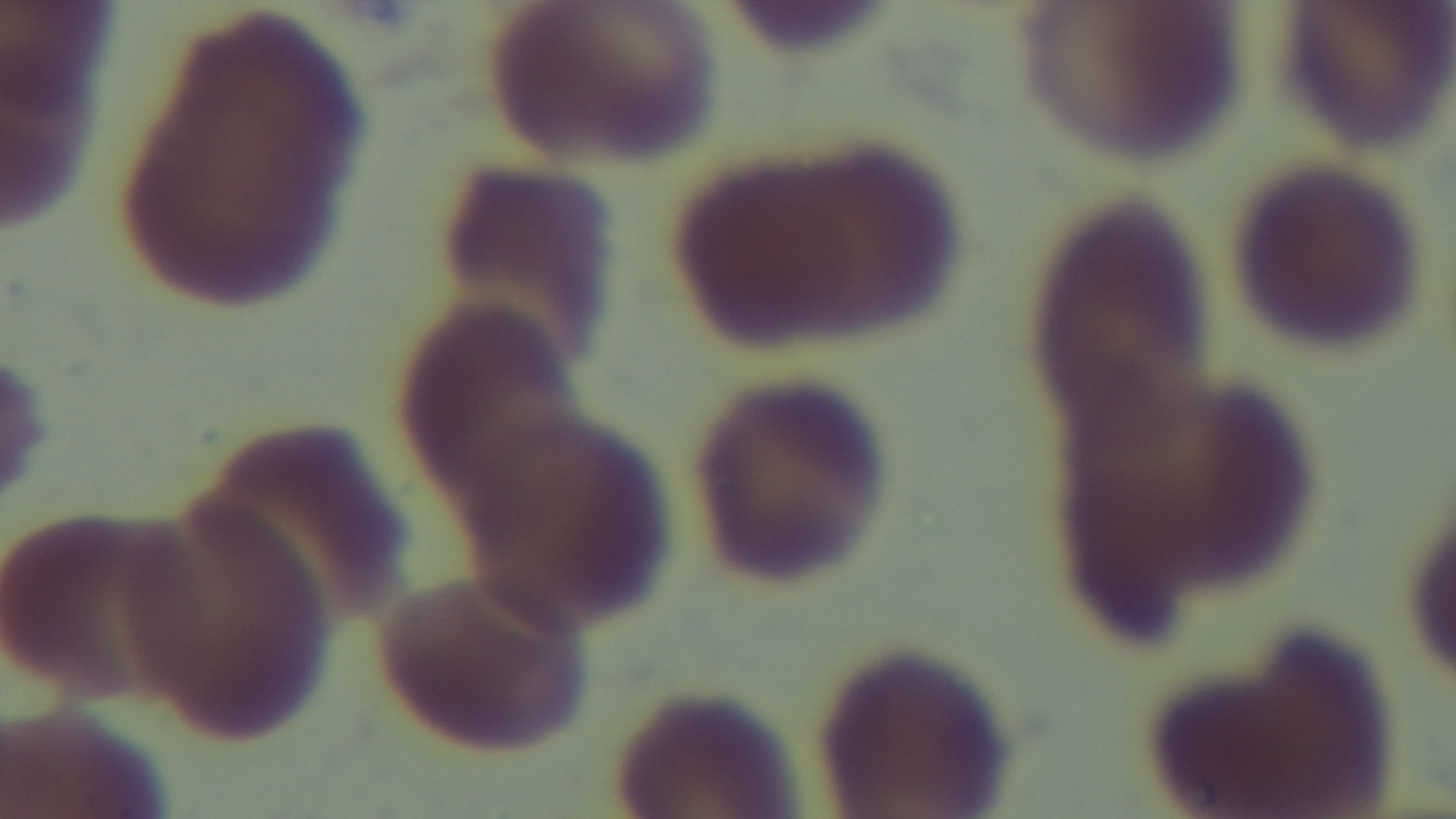
Malaria status: uninfected. Photomicrograph. Giemsa-stained. Preparation: thin. Single field of view. 100x oil-immersion objective. Mounted 4K digital camera.